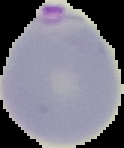 Malaria status: parasitized. From a thin blood smear. Cell region segmented out of the field of view; the surrounding area is masked to black. Image is 124×148 pixels.